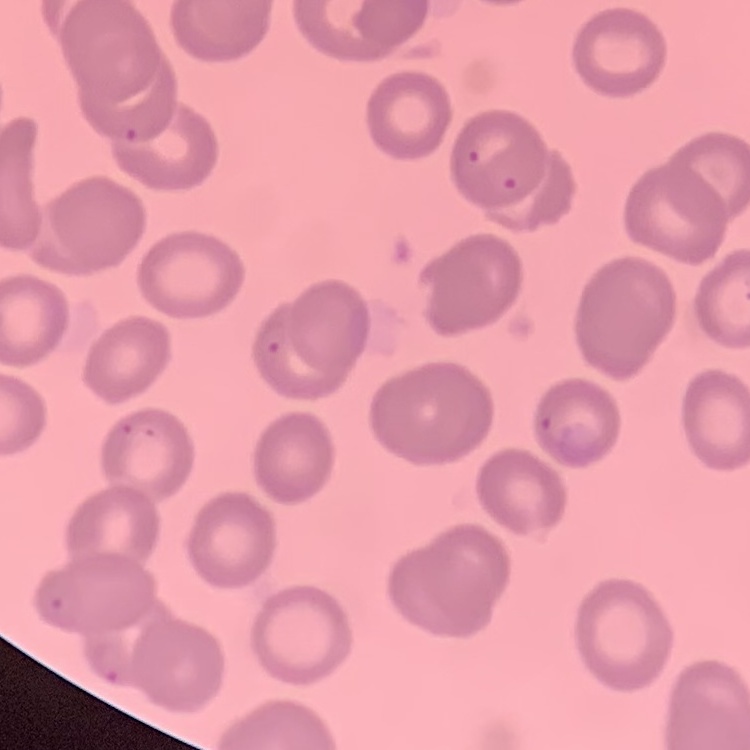

The erythrocytes exhibit no rouleaux formation. Field's or Giemsa stain. One tile cut from a larger photomicrograph. Thin peripheral smear.